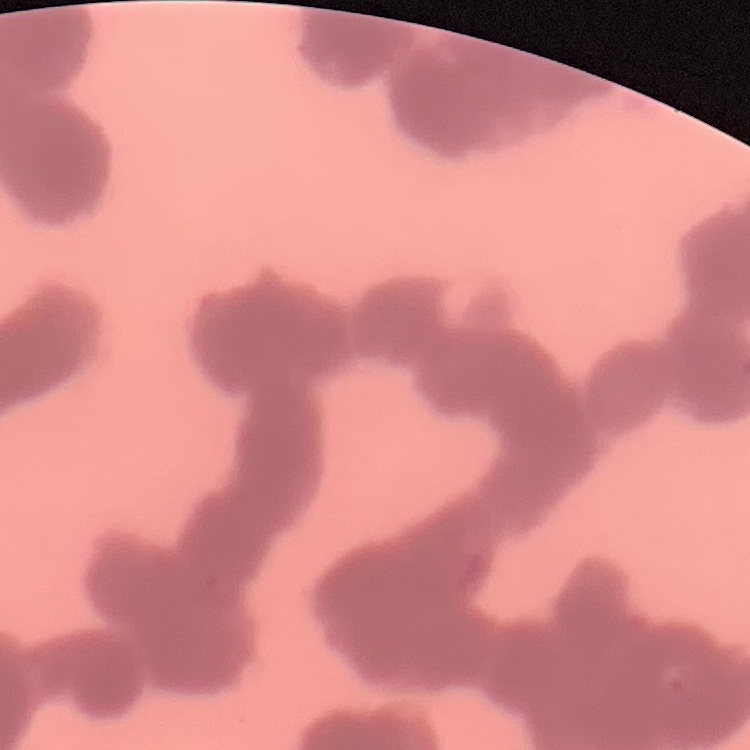

red_blood_cell_morphology: rouleaux formation
image_type: one tile cut from a larger photomicrograph
preparation: thin blood smear
stain: Field's or Giemsa